State which cell type is depicted.
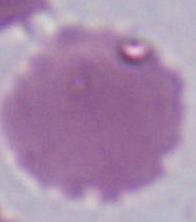
An erythrocyte.

Summary:
  - Magnification: 1000x
  - Modality: photomicrograph